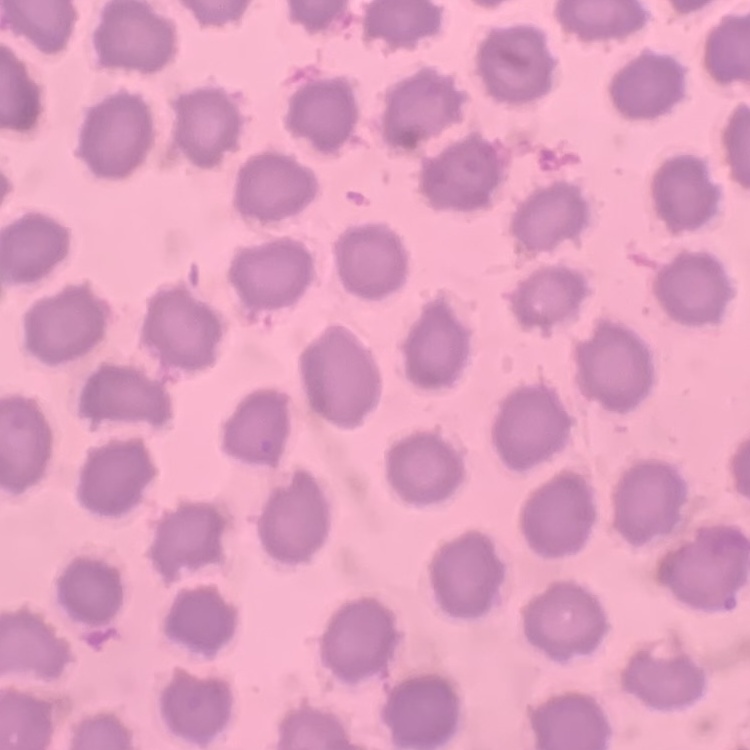

{
  "red_blood_cell_morphology": "no rouleaux formation",
  "image_type": "square crop of a larger photomicrograph",
  "preparation": "thin peripheral smear",
  "stain": "Field's or Giemsa"
}